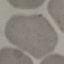

result: negative for malaria parasites
stain: Giemsa
capture: smartphone through the microscope eyepiece
image_type: cell patch, automatically extracted from a larger field of view and resized to 64 × 64 pixels
preparation: thin smear